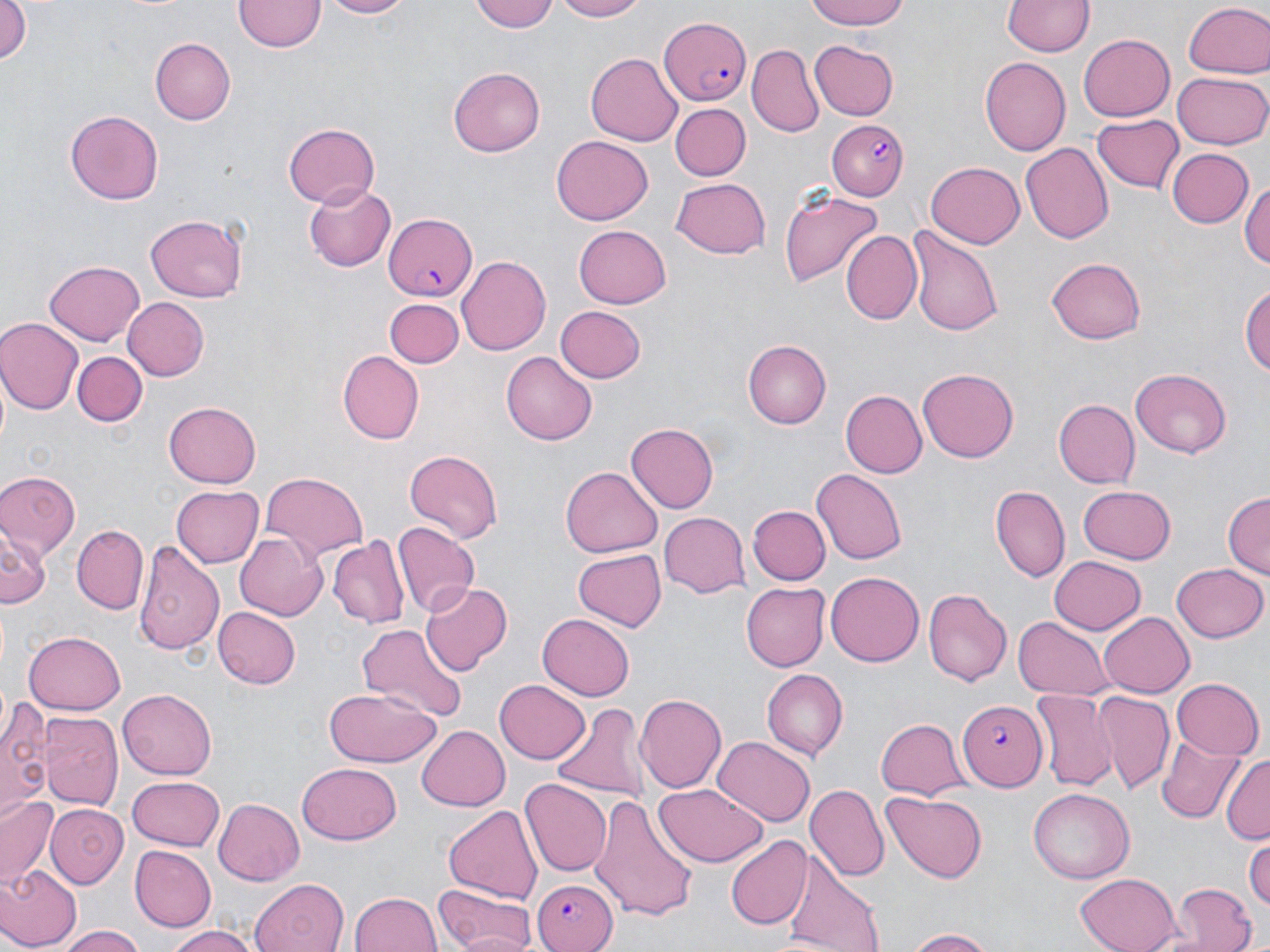

Summary:
  - Coordinate format: approximate bounding boxes as [x1, y1, x2, y2] in pixels
  - Uninfected red blood cell locations: [0, 0, 31, 73], [233, 0, 325, 53], [321, 0, 417, 19], [470, 0, 559, 32], [548, 0, 650, 22], [803, 0, 912, 32], [1002, 0, 1098, 57], [1183, 3, 1270, 79], [1078, 35, 1174, 120], [151, 38, 236, 124], [809, 40, 900, 120], [747, 45, 824, 138], [586, 50, 683, 144], [979, 56, 1070, 157], [449, 67, 546, 157], [1173, 71, 1269, 148], [669, 103, 749, 181], [65, 110, 164, 204], [1091, 114, 1183, 196], [283, 122, 380, 207], [549, 135, 653, 225], [1021, 142, 1114, 243], [1167, 147, 1253, 229], [926, 159, 1024, 246], [670, 178, 772, 259], [1242, 180, 1270, 275], [302, 183, 398, 274], [778, 188, 881, 289], [143, 212, 250, 302], [574, 225, 672, 308], [904, 227, 1003, 337], [840, 231, 923, 327], [457, 256, 551, 355], [1047, 258, 1146, 344], [43, 260, 146, 346], [1242, 281, 1270, 381], [122, 296, 209, 380], [383, 299, 463, 369], [555, 306, 647, 384], [0, 316, 82, 412], [742, 340, 832, 428], [338, 350, 424, 443], [502, 350, 596, 442], [72, 352, 145, 426], [1130, 367, 1233, 459], [918, 369, 1019, 463], [841, 390, 926, 478], [1053, 399, 1140, 487], [163, 401, 262, 487], [626, 423, 718, 514], [402, 448, 503, 543], [561, 466, 662, 557], [811, 469, 908, 564], [0, 471, 82, 559], [257, 471, 370, 559], [1077, 484, 1177, 564], [172, 485, 263, 567], [992, 486, 1069, 581], [1222, 492, 1269, 581], [748, 505, 829, 586], [659, 511, 749, 597], [393, 523, 479, 616], [0, 525, 46, 613], [72, 525, 147, 613], [234, 532, 327, 620], [328, 535, 409, 629], [134, 537, 226, 654], [572, 549, 667, 632], [1049, 555, 1146, 634], [1172, 563, 1267, 644], [825, 571, 926, 666], [421, 581, 510, 674], [740, 582, 829, 671], [922, 588, 1011, 687], [214, 607, 300, 688], [1100, 610, 1195, 695], [538, 612, 635, 699], [1013, 615, 1115, 700], [356, 621, 467, 724], [24, 630, 125, 714], [760, 669, 846, 759], [1170, 677, 1263, 758], [494, 678, 591, 765], [119, 688, 217, 778], [324, 690, 445, 770], [1031, 691, 1117, 790], [1091, 691, 1176, 796], [633, 692, 725, 795], [2, 698, 51, 819], [549, 703, 648, 804], [39, 710, 122, 812], [874, 716, 968, 800], [417, 725, 510, 809], [1156, 735, 1245, 823], [712, 737, 814, 826], [1222, 755, 1269, 845], [295, 764, 401, 845], [127, 775, 226, 851], [519, 778, 610, 876], [656, 783, 767, 868], [807, 784, 889, 885], [1027, 788, 1134, 885], [881, 793, 986, 882], [589, 795, 699, 921], [1, 796, 62, 887], [213, 797, 305, 885], [442, 803, 543, 904], [44, 804, 129, 889], [724, 836, 812, 930], [1245, 836, 1270, 911], [129, 846, 217, 932], [780, 857, 885, 950], [0, 864, 79, 950], [1076, 872, 1181, 952], [250, 878, 350, 952], [1171, 883, 1257, 952], [435, 885, 535, 952], [350, 890, 443, 952], [163, 925, 260, 952], [61, 927, 149, 952], [900, 928, 1001, 950]
  - Plasmodium falciparum-infected red blood cell locations: [658, 15, 752, 104], [828, 117, 910, 201], [382, 211, 478, 300], [960, 702, 1048, 789], [531, 877, 618, 952]
  - Slide-level diagnosis: Plasmodium falciparum
  - Stain: May-Grünwald-Giemsa
  - Field of view: one of a larger specimen
  - Modality: light microscopy
  - Preparation: thin blood smear
  - Magnification: 1000x
  - Image size: 1270×952 pixels